Outline each blood parasite and name the species.
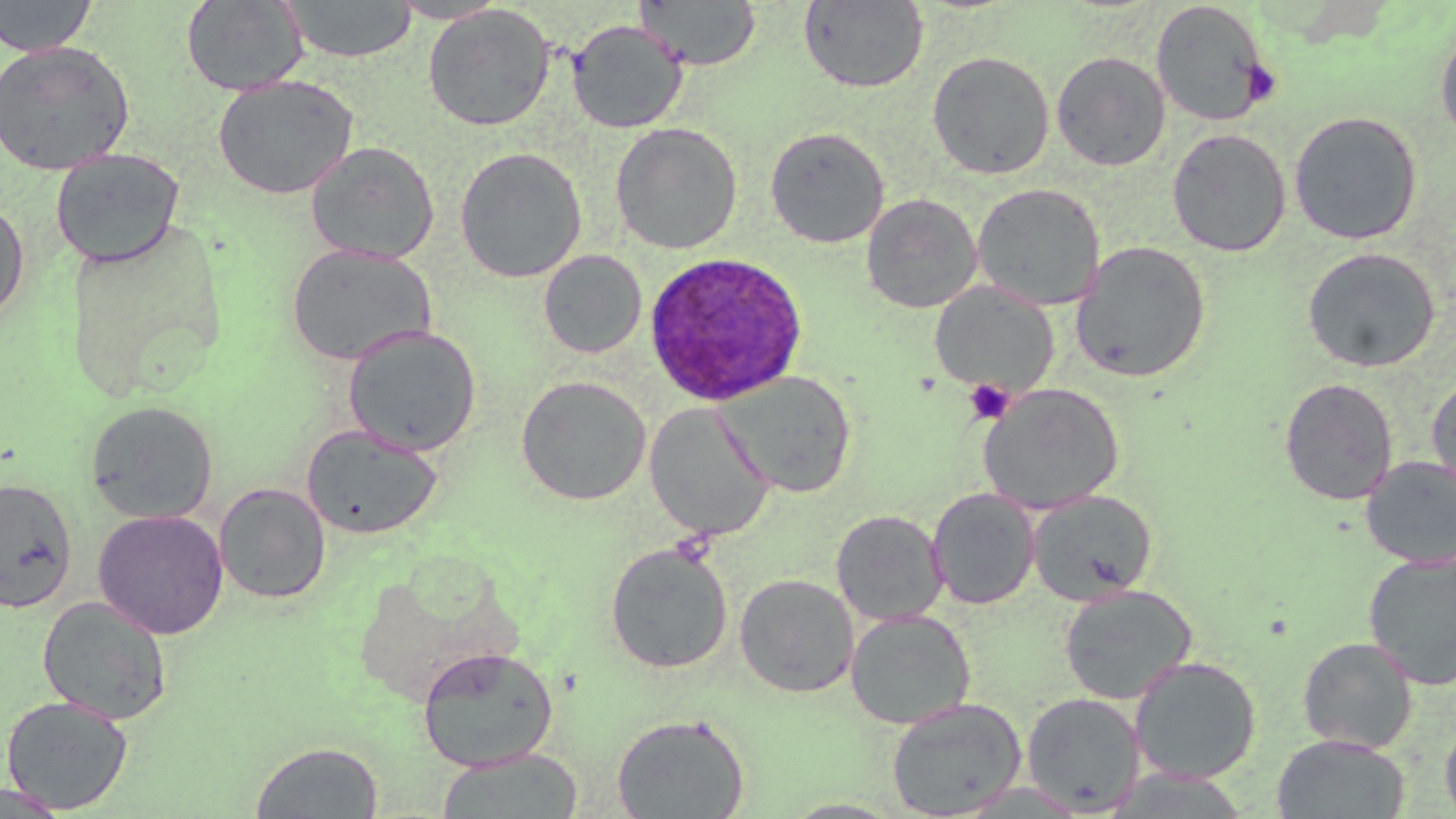
Approximate bounding boxes as named x1/y1/x2/y2 corners in pixels.
Plasmodium ovale-infected red blood cells: (x1=643, y1=251, x2=808, y2=407).
No Plasmodium falciparum, Plasmodium malariae, Plasmodium vivax, Babesia divergens, or Trypanosoma brucei observed.

Summary:
  - Platelet locations: (x1=1240, y1=59, x2=1281, y2=106), (x1=964, y1=379, x2=1015, y2=424)
  - Uninfected red blood cell locations: (x1=0, y1=0, x2=98, y2=57), (x1=181, y1=0, x2=309, y2=96), (x1=388, y1=0, x2=509, y2=24), (x1=635, y1=0, x2=761, y2=71), (x1=282, y1=1, x2=417, y2=63), (x1=798, y1=1, x2=928, y2=93), (x1=1150, y1=2, x2=1272, y2=127), (x1=422, y1=4, x2=556, y2=131), (x1=567, y1=19, x2=688, y2=134), (x1=1435, y1=23, x2=1456, y2=144), (x1=0, y1=40, x2=135, y2=176), (x1=927, y1=51, x2=1055, y2=180), (x1=1051, y1=51, x2=1171, y2=171), (x1=213, y1=75, x2=359, y2=199), (x1=1288, y1=110, x2=1424, y2=245), (x1=610, y1=123, x2=743, y2=254), (x1=765, y1=126, x2=890, y2=248), (x1=1167, y1=128, x2=1291, y2=256), (x1=306, y1=141, x2=439, y2=265), (x1=454, y1=147, x2=588, y2=283), (x1=49, y1=148, x2=185, y2=269), (x1=972, y1=183, x2=1105, y2=311), (x1=861, y1=193, x2=983, y2=313), (x1=0, y1=199, x2=30, y2=324), (x1=1070, y1=241, x2=1211, y2=383), (x1=285, y1=242, x2=436, y2=367), (x1=1302, y1=246, x2=1441, y2=373), (x1=538, y1=250, x2=647, y2=358), (x1=930, y1=281, x2=1059, y2=397), (x1=342, y1=324, x2=482, y2=456), (x1=717, y1=370, x2=857, y2=497), (x1=1427, y1=373, x2=1456, y2=500), (x1=515, y1=375, x2=652, y2=506), (x1=1279, y1=377, x2=1398, y2=505), (x1=978, y1=383, x2=1125, y2=514), (x1=85, y1=400, x2=219, y2=524), (x1=644, y1=402, x2=775, y2=541), (x1=301, y1=424, x2=444, y2=540), (x1=1360, y1=455, x2=1456, y2=569), (x1=0, y1=477, x2=79, y2=613), (x1=213, y1=482, x2=331, y2=604), (x1=927, y1=488, x2=1040, y2=609), (x1=1027, y1=489, x2=1159, y2=605), (x1=92, y1=509, x2=229, y2=639), (x1=831, y1=509, x2=948, y2=625), (x1=605, y1=542, x2=734, y2=674), (x1=1363, y1=551, x2=1456, y2=691), (x1=734, y1=573, x2=859, y2=698), (x1=1058, y1=584, x2=1198, y2=705), (x1=37, y1=595, x2=173, y2=724), (x1=845, y1=608, x2=976, y2=729), (x1=1298, y1=637, x2=1418, y2=754), (x1=417, y1=647, x2=558, y2=770), (x1=1129, y1=655, x2=1262, y2=784), (x1=1021, y1=691, x2=1146, y2=815), (x1=1, y1=695, x2=134, y2=814), (x1=885, y1=697, x2=1027, y2=817), (x1=611, y1=712, x2=751, y2=818), (x1=1440, y1=716, x2=1456, y2=819), (x1=1272, y1=734, x2=1411, y2=818), (x1=250, y1=741, x2=384, y2=818), (x1=435, y1=748, x2=584, y2=819), (x1=0, y1=784, x2=74, y2=818)
  - Slide-level diagnosis: Plasmodium ovale
  - Magnification: 1000x
  - Preparation: thin blood smear
  - Modality: optical microscopy
  - Image size: 1456×819 pixels
  - Stain: May-Grünwald-Giemsa
  - Field of view: one of a larger specimen